Identify the parasite.
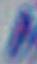

This is Toxoplasma gondii.

modality = micrograph
magnification = 1000x